Give the position of every malaria parasite.
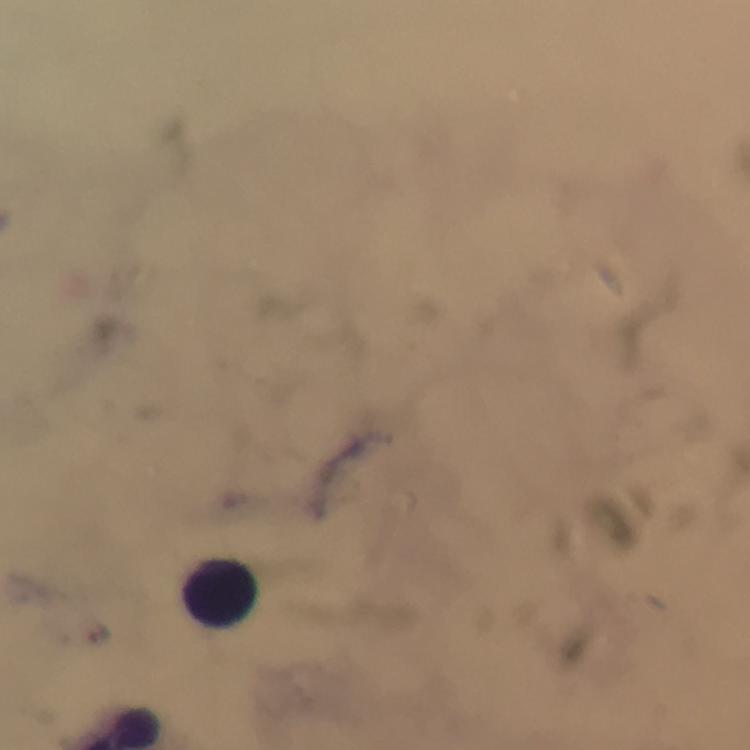
Approximate centers as [x, y] in pixels.
Malaria parasites: [99, 631].

Summary:
  - Leukocyte locations: [221, 592]
  - Immersion oil: used
  - Cropped from: one field of view
  - Context: from a diagnostic examination for malaria
  - Image size: 750×750 pixels
  - Magnification: 100x
  - Preparation: thick blood smear
  - Capture: smartphone mounted on the microscope
  - Stain: Giemsa